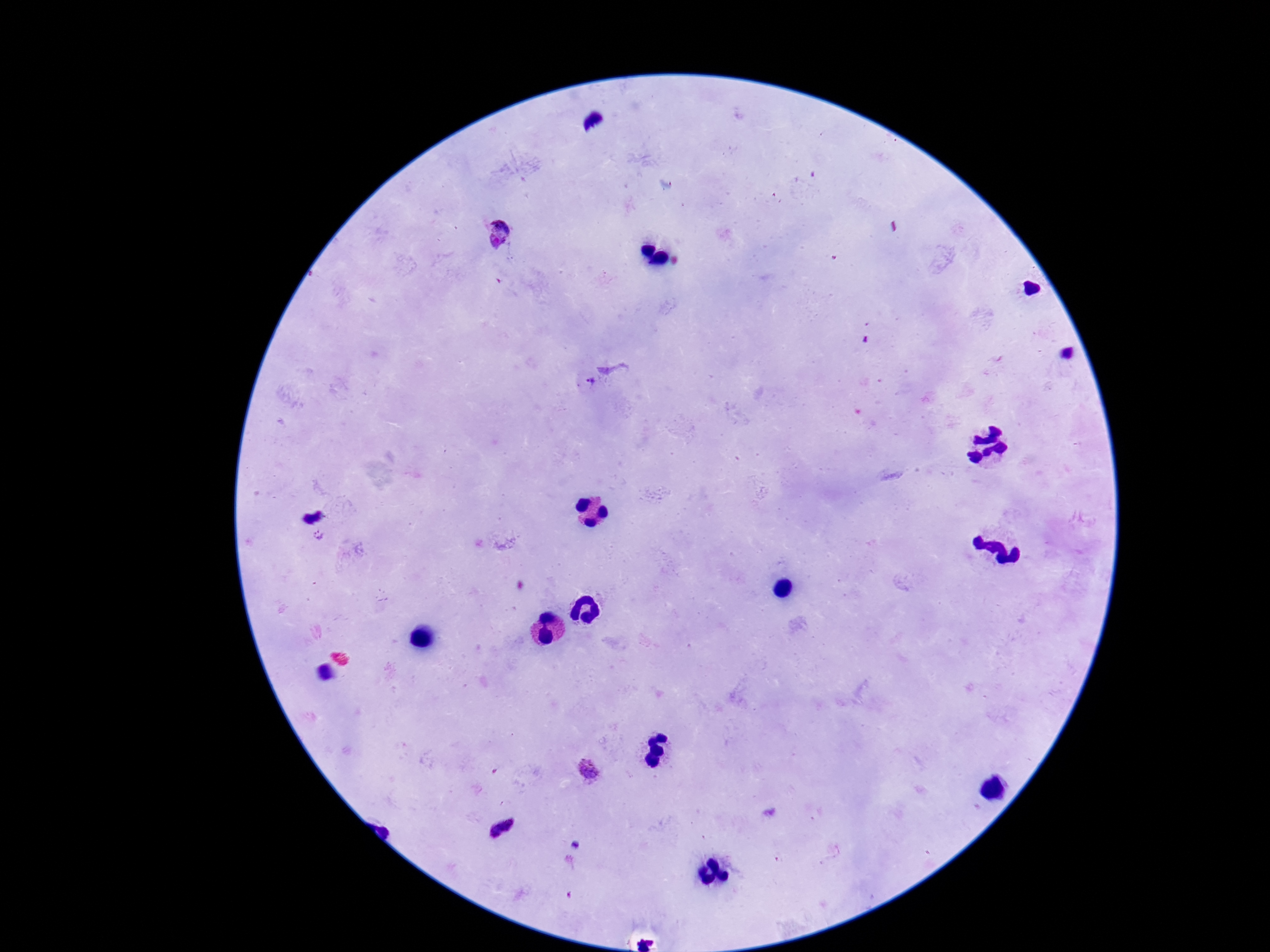
Approximate object centers, in pixels from the top-left corner. Plasmodium parasite locations: (x=498, y=235), (x=590, y=382), (x=590, y=766), (x=501, y=827). Patient malaria status: infected. Smartphone photograph taken through the microscope eyepiece. Image is 1270×952 pixels. Single field of view. Thick blood smear. 100x magnification. Giemsa-stained preparation.